Assess the morphology of the erythrocytes.
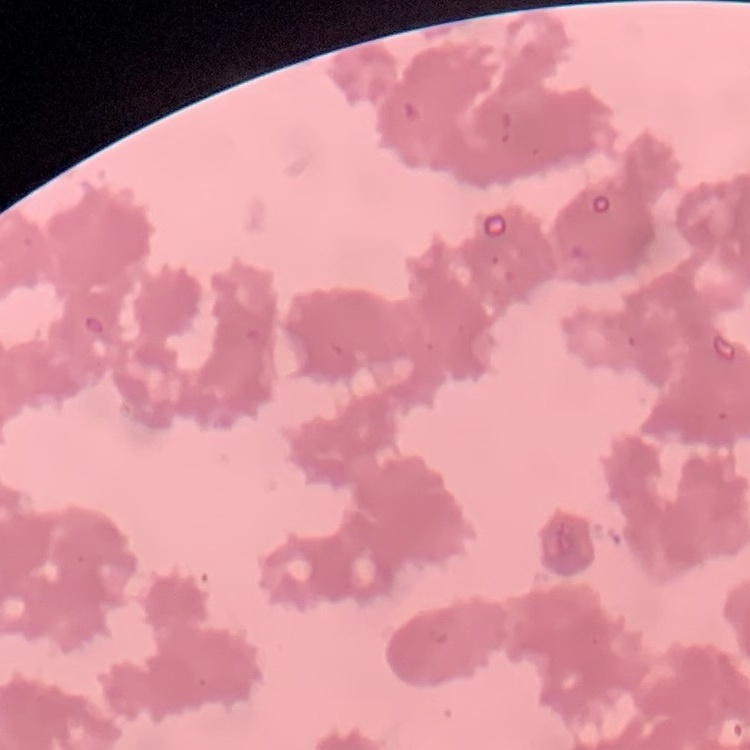
Rouleaux formation.

Field's or Giemsa stain. One tile cut from a larger photomicrograph. Thin blood smear.